Identify the preparation type.
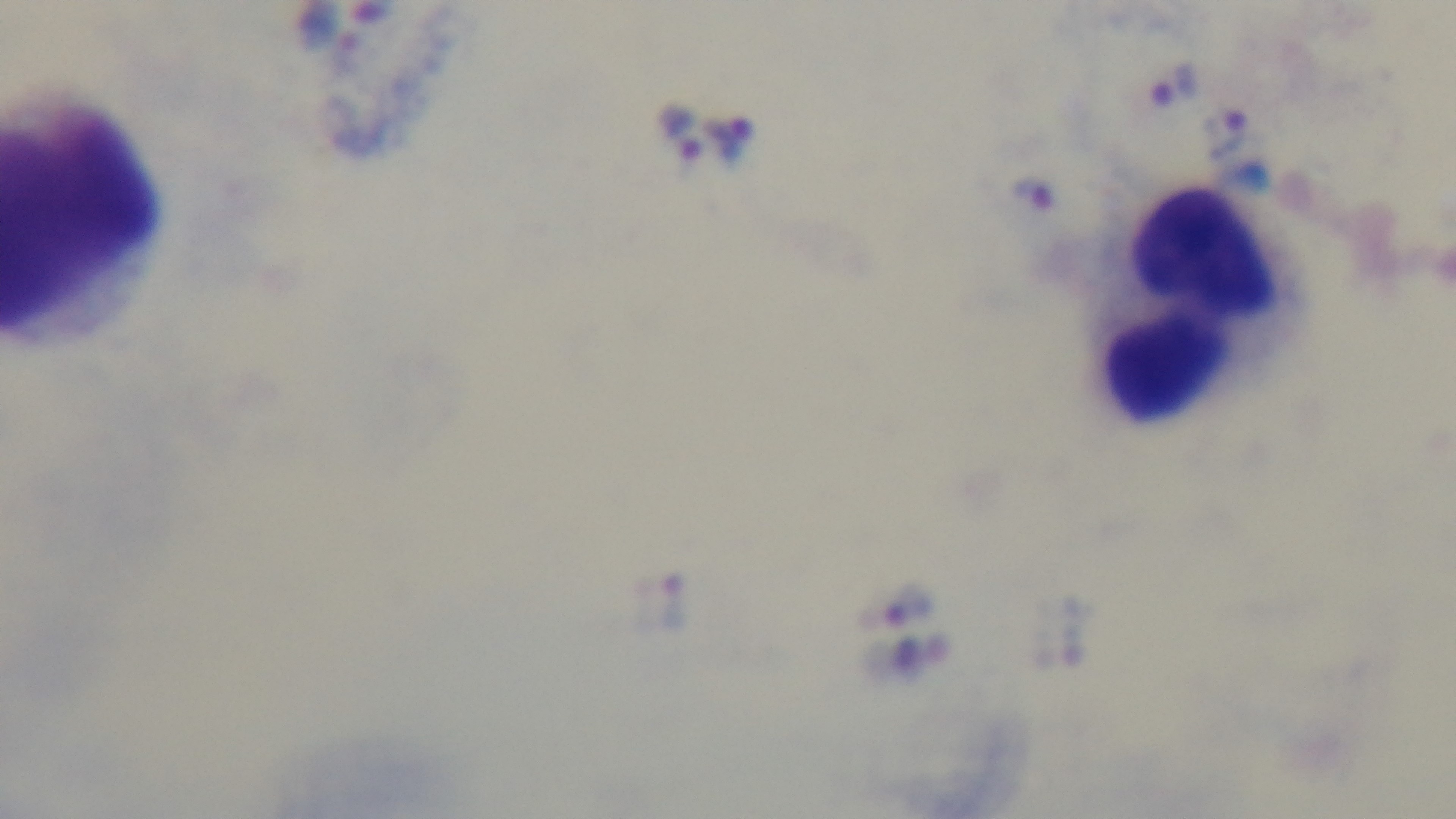
Thick.

Summary:
  - Stain: Giemsa
  - Field of view: single
  - Objective: 100x oil immersion
  - Capture: mounted 4K digital camera
  - Modality: light microscopy
  - Malaria status: infected